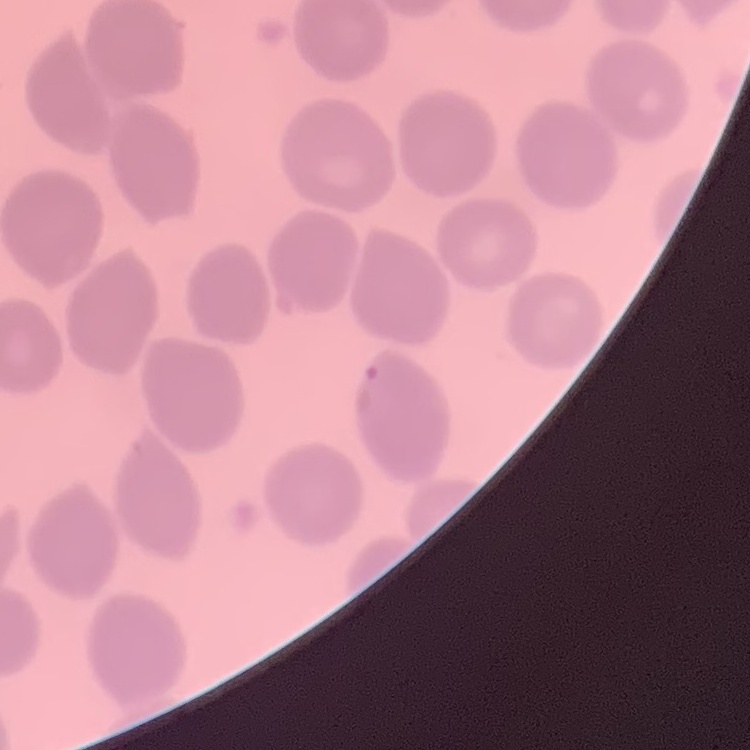

Summary:
  - Red blood cell morphology: no rouleaux formation
  - Image type: square crop of a larger photomicrograph
  - Preparation: thin peripheral smear
  - Stain: Field's or Giemsa